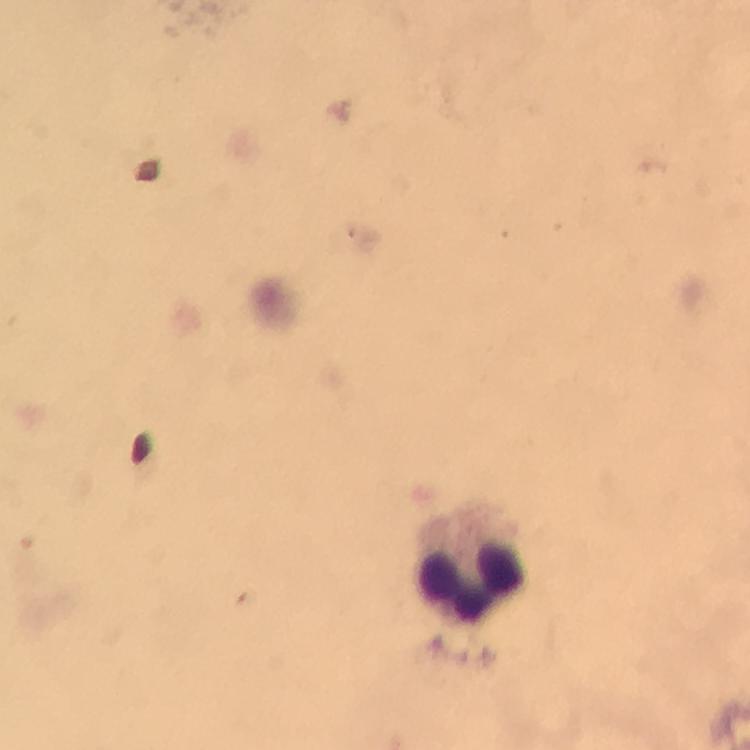

immersion oil = applied
capture = smartphone photograph through a microscope
context = from a malaria diagnostic workup
magnification = 100x
cropped from = a single field of view
preparation = thick blood film
stain = Giemsa
image size = 750×750 pixels
leukocyte locations = approximate centers as {x, y} in pixels: {473, 568}
Plasmodium parasites = none detected